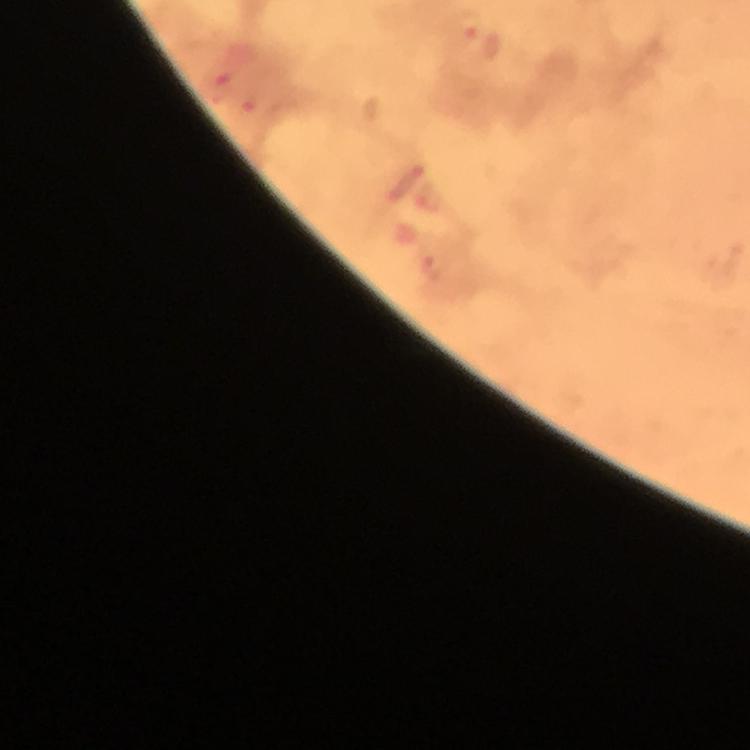

Approximate centers as [x, y] in pixels. Malaria parasite locations: [480, 39], [219, 81], [252, 108], [403, 183], [428, 201], [433, 267]. 100x magnification. Cropped region of a single field of view. Image is 750×750 pixels. Photographed with a smartphone mounted on the microscope. From a diagnostic examination for malaria. Thick smear. Immersion oil was used. Giemsa stain.